Classify this cell by malaria status.
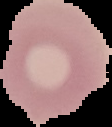

Uninfected.

Summary:
  - Image size: 112×127 pixels
  - Image type: segmented cell region on a black background
  - Preparation: thin blood film